Assess the morphology of the red blood cells.
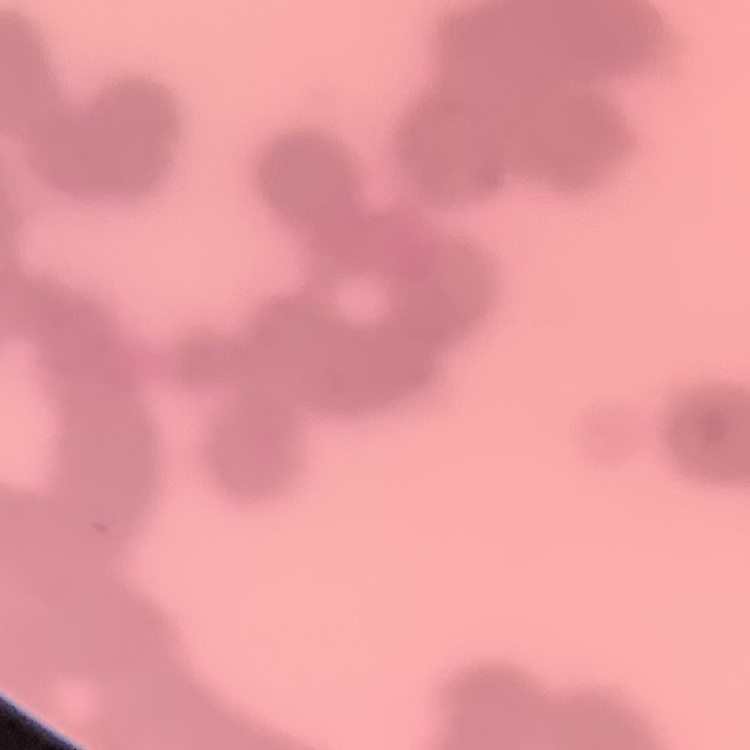

They show rouleaux formation.

preparation: thin blood film
image_type: square crop of a larger photomicrograph
stain: Field's or Giemsa